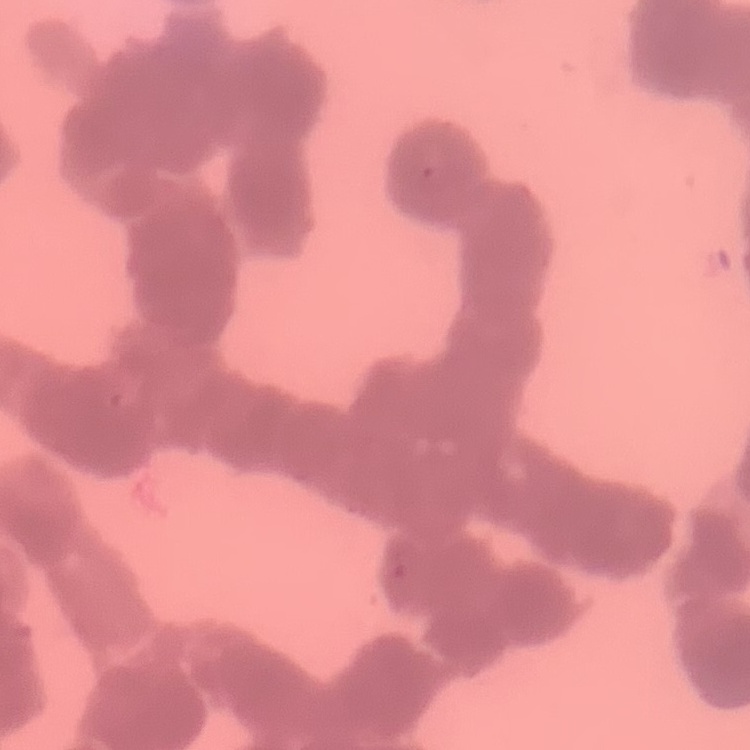
{
  "erythrocyte_morphology": "rouleaux formation",
  "preparation": "thin blood smear",
  "stain": "Field's or Giemsa",
  "image_type": "square crop of a larger photomicrograph"
}